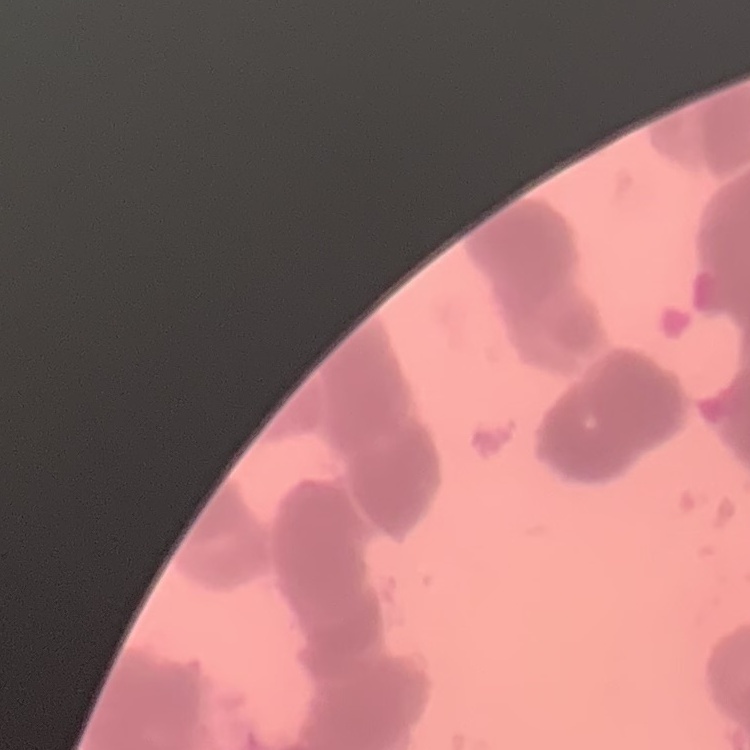
Summary:
  - Red blood cell morphology: rouleaux formation
  - Stain: Field's or Giemsa
  - Image type: one tile cut from a larger photomicrograph
  - Preparation: thin peripheral smear